Assess this cell for malaria.
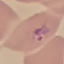

Parasitized.

preparation = thin blood film
capture = smartphone through the microscope eyepiece
stain = Giemsa
image type = automatically extracted cell patch, resized to 64 × 64 pixels